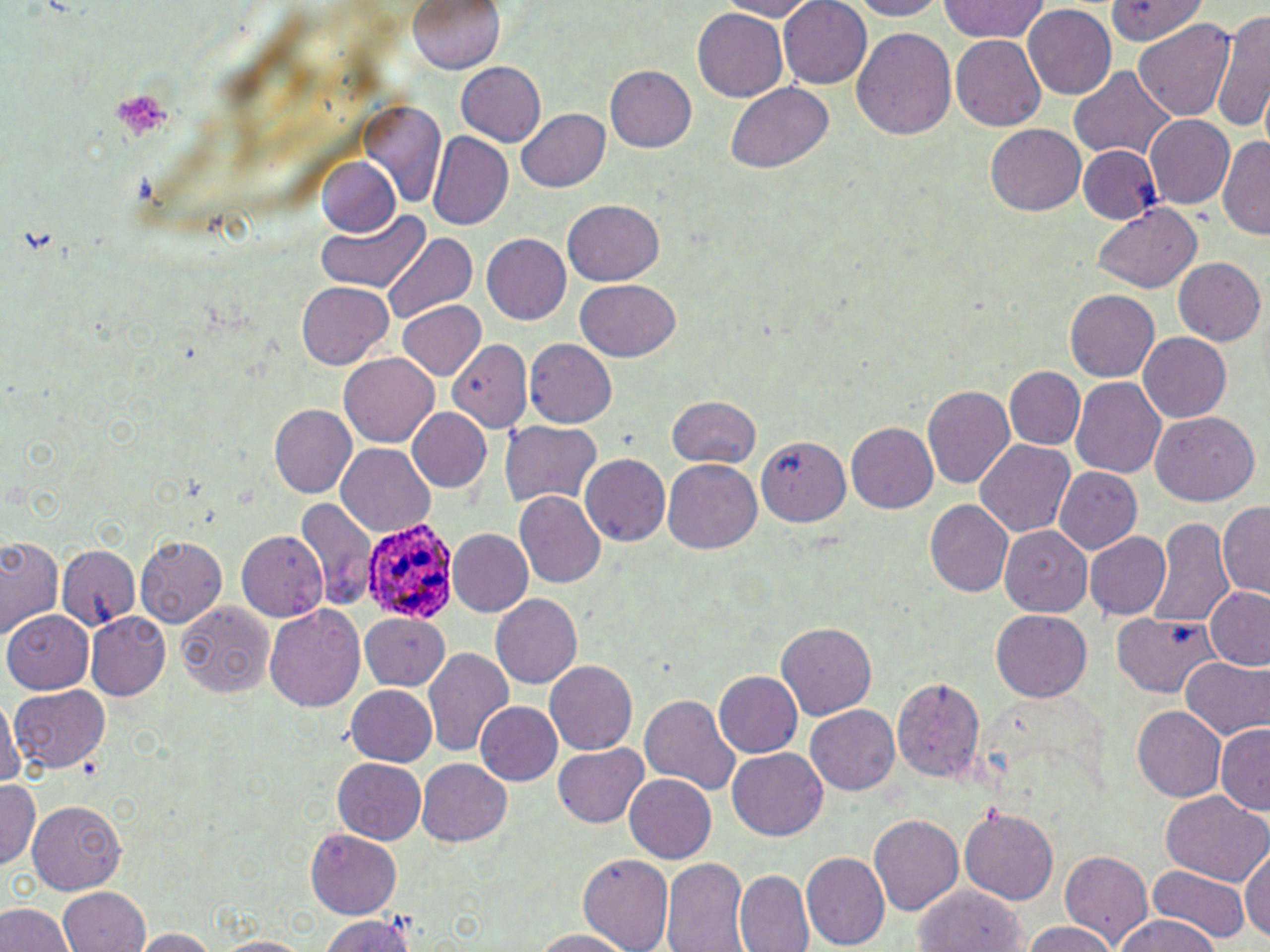
Summary:
  - Coordinate format: approximate bounding boxes as named x1/y1/x2/y2 corners in pixels
  - Platelet locations: (x1=112, y1=86, x2=175, y2=150)
  - Plasmodium ovale-infected red blood cell locations: (x1=362, y1=517, x2=457, y2=622)
  - Uninfected red blood cell locations: (x1=407, y1=0, x2=504, y2=76), (x1=709, y1=0, x2=826, y2=20), (x1=777, y1=0, x2=875, y2=88), (x1=842, y1=0, x2=951, y2=19), (x1=938, y1=0, x2=1052, y2=44), (x1=1107, y1=0, x2=1216, y2=49), (x1=1024, y1=5, x2=1115, y2=100), (x1=1214, y1=8, x2=1270, y2=137), (x1=692, y1=9, x2=787, y2=102), (x1=1134, y1=16, x2=1236, y2=123), (x1=851, y1=26, x2=956, y2=142), (x1=950, y1=33, x2=1046, y2=132), (x1=454, y1=62, x2=547, y2=146), (x1=1068, y1=64, x2=1175, y2=165), (x1=605, y1=67, x2=697, y2=153), (x1=728, y1=81, x2=835, y2=173), (x1=360, y1=104, x2=446, y2=208), (x1=517, y1=108, x2=608, y2=192), (x1=1144, y1=115, x2=1234, y2=209), (x1=987, y1=124, x2=1085, y2=217), (x1=1218, y1=133, x2=1270, y2=242), (x1=426, y1=134, x2=512, y2=233), (x1=1079, y1=145, x2=1161, y2=224), (x1=315, y1=156, x2=402, y2=240), (x1=562, y1=199, x2=664, y2=284), (x1=1092, y1=204, x2=1202, y2=294), (x1=315, y1=211, x2=430, y2=294), (x1=384, y1=232, x2=474, y2=321), (x1=483, y1=233, x2=572, y2=325), (x1=1172, y1=258, x2=1263, y2=347), (x1=576, y1=280, x2=680, y2=361), (x1=297, y1=282, x2=392, y2=369), (x1=1065, y1=291, x2=1160, y2=382), (x1=396, y1=300, x2=484, y2=379), (x1=1137, y1=332, x2=1231, y2=423), (x1=447, y1=339, x2=532, y2=431), (x1=525, y1=339, x2=618, y2=428), (x1=341, y1=353, x2=438, y2=446), (x1=1006, y1=366, x2=1085, y2=450), (x1=1070, y1=375, x2=1165, y2=476), (x1=923, y1=385, x2=1015, y2=491), (x1=668, y1=395, x2=762, y2=468), (x1=268, y1=404, x2=357, y2=499), (x1=407, y1=407, x2=495, y2=495), (x1=1149, y1=411, x2=1260, y2=505), (x1=500, y1=421, x2=602, y2=510), (x1=846, y1=422, x2=939, y2=514), (x1=757, y1=433, x2=850, y2=527), (x1=973, y1=440, x2=1074, y2=539), (x1=338, y1=445, x2=436, y2=537), (x1=579, y1=453, x2=670, y2=548), (x1=664, y1=460, x2=762, y2=554), (x1=1055, y1=467, x2=1142, y2=552), (x1=515, y1=491, x2=606, y2=589), (x1=295, y1=498, x2=375, y2=610), (x1=926, y1=500, x2=1014, y2=596), (x1=1219, y1=500, x2=1269, y2=601), (x1=1149, y1=517, x2=1233, y2=627), (x1=1001, y1=527, x2=1092, y2=618), (x1=447, y1=528, x2=533, y2=617), (x1=236, y1=531, x2=327, y2=621), (x1=1085, y1=533, x2=1169, y2=618), (x1=135, y1=536, x2=228, y2=628), (x1=0, y1=537, x2=62, y2=640), (x1=56, y1=542, x2=142, y2=627), (x1=1203, y1=586, x2=1270, y2=672), (x1=490, y1=593, x2=584, y2=690), (x1=173, y1=602, x2=276, y2=696), (x1=264, y1=604, x2=366, y2=714), (x1=359, y1=610, x2=452, y2=689), (x1=87, y1=612, x2=171, y2=700), (x1=990, y1=612, x2=1090, y2=702), (x1=1112, y1=612, x2=1225, y2=699), (x1=5, y1=613, x2=94, y2=695), (x1=776, y1=621, x2=878, y2=718), (x1=424, y1=646, x2=514, y2=759), (x1=1178, y1=656, x2=1269, y2=740), (x1=545, y1=661, x2=638, y2=755), (x1=713, y1=671, x2=801, y2=759), (x1=889, y1=675, x2=985, y2=781), (x1=344, y1=685, x2=436, y2=766), (x1=9, y1=686, x2=114, y2=777), (x1=638, y1=689, x2=741, y2=796), (x1=0, y1=695, x2=20, y2=791), (x1=473, y1=702, x2=561, y2=787), (x1=806, y1=706, x2=899, y2=795), (x1=1132, y1=706, x2=1227, y2=801), (x1=1215, y1=724, x2=1270, y2=816), (x1=551, y1=743, x2=649, y2=829), (x1=727, y1=749, x2=828, y2=841), (x1=332, y1=757, x2=428, y2=842), (x1=416, y1=758, x2=513, y2=847), (x1=624, y1=773, x2=716, y2=864), (x1=0, y1=780, x2=41, y2=871), (x1=1159, y1=793, x2=1268, y2=886), (x1=27, y1=799, x2=127, y2=894), (x1=959, y1=804, x2=1058, y2=903), (x1=868, y1=813, x2=964, y2=918), (x1=305, y1=830, x2=402, y2=915), (x1=1240, y1=845, x2=1270, y2=946), (x1=804, y1=852, x2=889, y2=950), (x1=1061, y1=852, x2=1155, y2=948), (x1=579, y1=853, x2=673, y2=952), (x1=661, y1=858, x2=749, y2=952), (x1=313, y1=866, x2=407, y2=952), (x1=1140, y1=868, x2=1249, y2=945), (x1=736, y1=870, x2=813, y2=951), (x1=913, y1=884, x2=1027, y2=952), (x1=56, y1=888, x2=151, y2=952), (x1=0, y1=901, x2=73, y2=952), (x1=313, y1=913, x2=419, y2=952), (x1=1107, y1=916, x2=1226, y2=952), (x1=1018, y1=921, x2=1120, y2=952), (x1=522, y1=927, x2=641, y2=950), (x1=132, y1=928, x2=219, y2=952), (x1=206, y1=935, x2=318, y2=952)
  - Slide-level diagnosis: Plasmodium ovale
  - Field of view: one of a larger specimen
  - Stain: May-Grünwald-Giemsa
  - Image size: 1270×952 pixels
  - Preparation: thin blood smear
  - Magnification: 1000x
  - Modality: optical microscopy